Comment on the morphology of the erythrocytes.
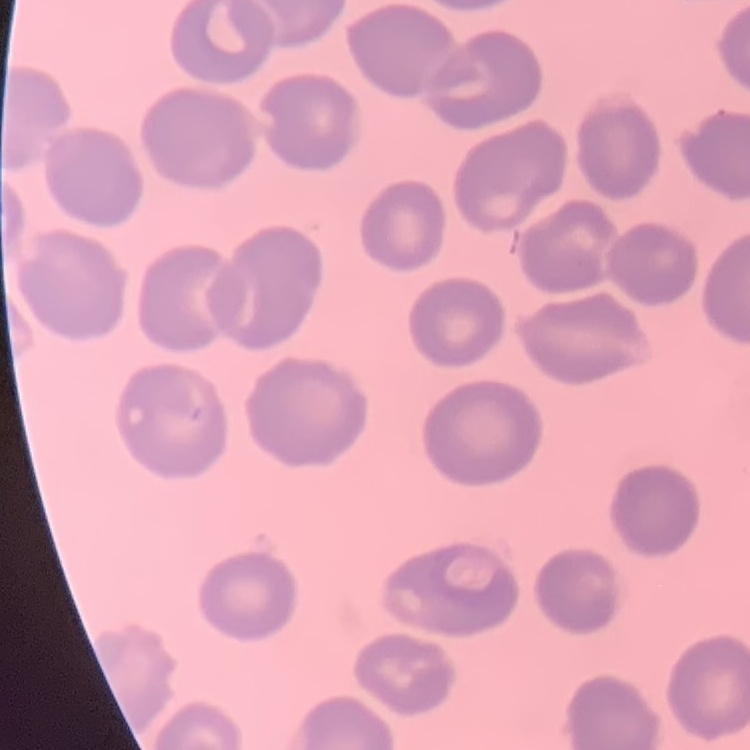
They show no rouleaux formation.

Summary:
  - Image type: one tile cut from a larger photomicrograph
  - Preparation: thin blood smear
  - Stain: Field's or Giemsa